Name the blood parasite species.
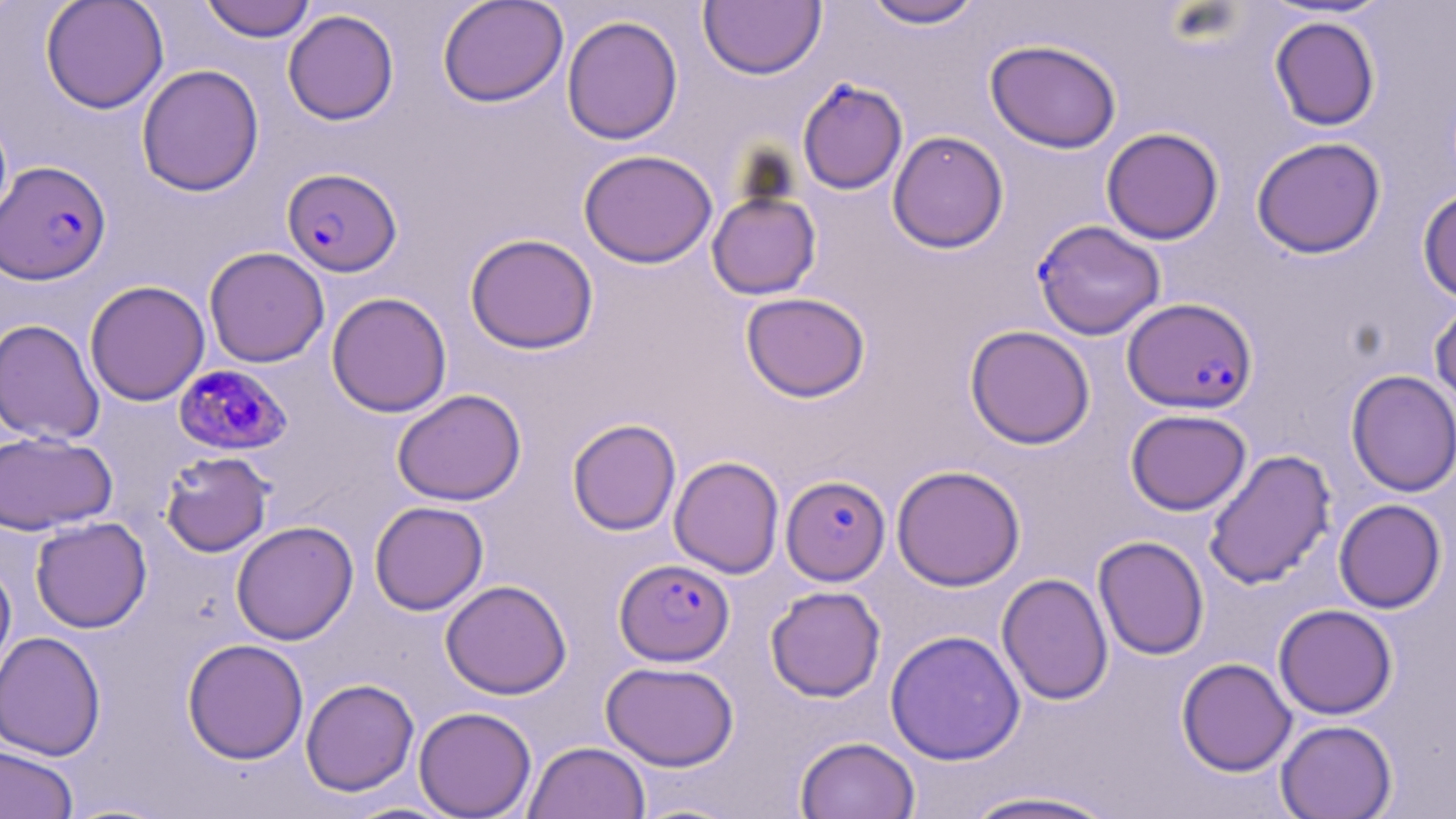
Plasmodium falciparum.

Approximate bounding boxes as [x1, y1, x2, y2] in pixels. Uninfected red blood cell locations: [40, 0, 169, 113], [199, 0, 317, 42], [437, 0, 569, 108], [861, 0, 985, 29], [699, 1, 826, 80], [283, 9, 400, 125], [561, 14, 683, 145], [1269, 16, 1381, 131], [984, 38, 1122, 154], [136, 64, 264, 196], [1101, 127, 1224, 245], [887, 130, 1009, 253], [1251, 136, 1386, 259], [578, 149, 717, 268], [1417, 187, 1456, 304], [707, 190, 821, 300], [464, 232, 599, 354], [204, 247, 330, 368], [84, 280, 210, 406], [326, 292, 452, 418], [741, 292, 870, 402], [1429, 299, 1456, 411], [0, 318, 105, 445], [965, 325, 1095, 449], [1346, 370, 1456, 497], [392, 389, 526, 506], [1125, 409, 1251, 515], [567, 418, 681, 536], [0, 430, 117, 535], [1203, 449, 1337, 590], [160, 451, 274, 557], [669, 456, 784, 578], [891, 465, 1026, 591], [1333, 499, 1447, 613], [369, 501, 489, 615], [30, 516, 152, 633], [231, 520, 358, 645], [1093, 535, 1210, 660], [0, 559, 16, 688], [997, 573, 1113, 705], [440, 579, 572, 699], [765, 586, 886, 702], [1274, 604, 1398, 719], [885, 629, 1025, 765], [0, 631, 106, 760], [182, 638, 309, 764], [1176, 658, 1297, 776], [600, 660, 739, 771], [300, 678, 419, 797], [414, 706, 537, 818], [1275, 719, 1398, 819], [795, 736, 920, 819], [523, 741, 650, 819], [0, 743, 79, 818], [960, 789, 1121, 819]. Plasmodium falciparum-infected red blood cell locations: [797, 77, 908, 195], [1, 160, 111, 285], [282, 167, 402, 277], [1033, 220, 1165, 339], [1123, 297, 1258, 414], [174, 363, 292, 456], [781, 475, 890, 585], [615, 559, 735, 666]. Light microscopy. May-Grünwald-Giemsa stain. One field of a larger specimen. 1000x magnification. Image is 1456×819 pixels. Thin blood smear.